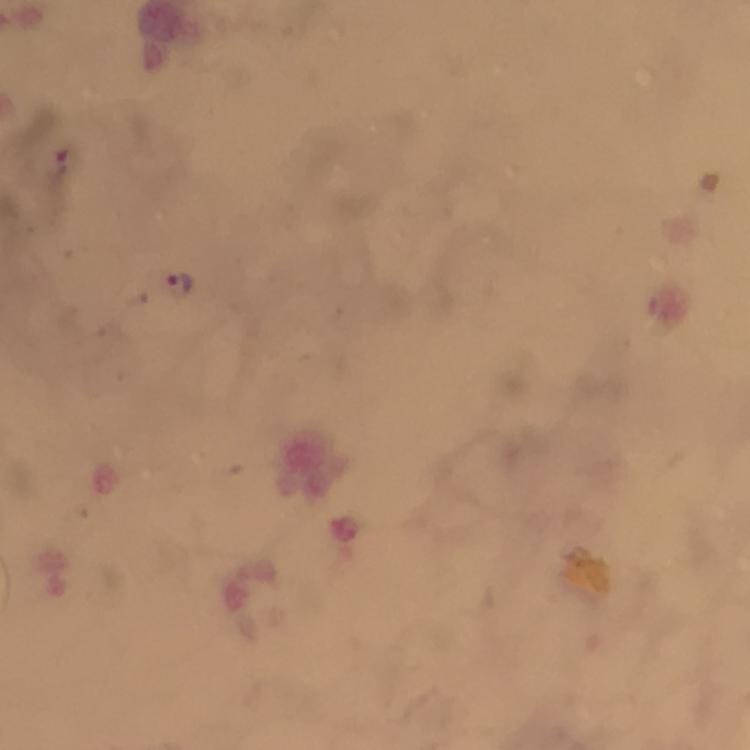
{
  "stain": "Giemsa",
  "cropped_from": "one field of view",
  "plasmodium_parasite_locations": "approximate object centers, in pixels from the top-left corner: (x=55, y=165), (x=181, y=285)",
  "image_size": "750×750 pixels",
  "context": "from a diagnostic examination for malaria",
  "preparation": "thick blood film",
  "capture": "smartphone camera through the microscope",
  "magnification": "100x",
  "immersion_oil": "applied"
}